Locate every white blood cell.
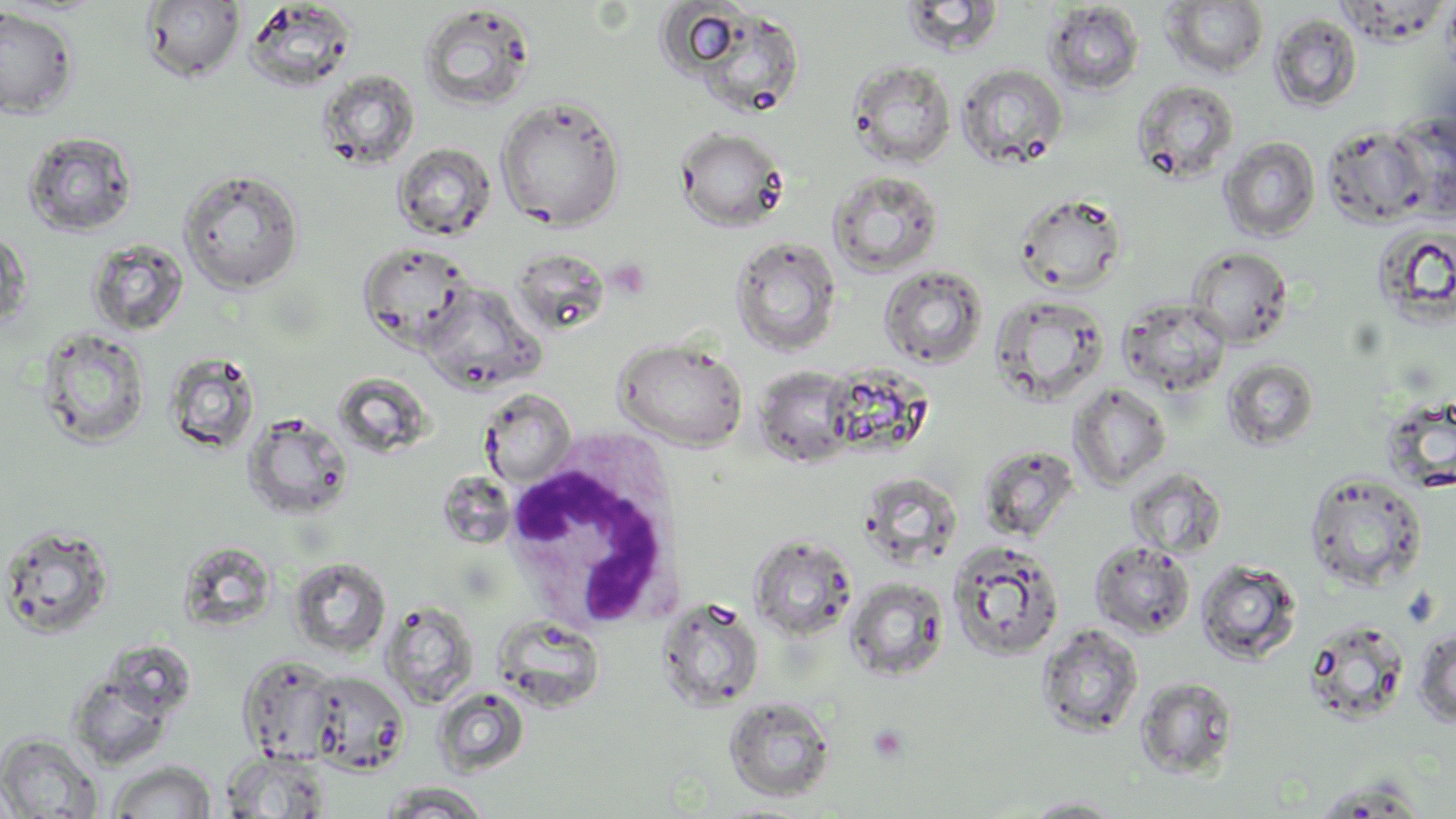
Approximate bounding boxes as (x1,y1)-(x2,y2) corner pairs in pixels.
White blood cells: (503,429)-(687,633).

slide-level diagnosis = no evidence of blood parasites
magnification = 1000x
stain = May-Grünwald-Giemsa
preparation = thin blood film
image size = 1456×819 pixels
field of view = one of a larger specimen
uninfected red blood cell locations = approximate bounding boxes as (x1,y1)-(x2,y2) corner pairs in pixels: (141,1)-(246,84), (244,1)-(358,94), (899,1)-(1007,57), (1161,1)-(1269,79), (1043,2)-(1145,95), (654,3)-(752,80), (417,4)-(537,112), (0,6)-(79,119), (683,7)-(807,119), (1269,13)-(1363,112), (847,59)-(956,169), (956,63)-(1068,170), (316,69)-(420,170), (1131,79)-(1240,184), (495,96)-(626,230), (1388,111)-(1456,220), (1321,125)-(1428,227), (673,126)-(789,231), (22,130)-(138,238), (1219,137)-(1320,241), (393,143)-(496,241), (178,168)-(305,294), (827,170)-(944,278), (1014,191)-(1128,295), (1372,224)-(1456,328), (0,226)-(33,333), (729,236)-(842,357), (86,238)-(189,337), (357,241)-(475,351), (1187,246)-(1294,349), (508,247)-(609,335), (878,265)-(989,370), (420,281)-(544,394), (989,292)-(1110,405), (1118,297)-(1231,396), (37,327)-(151,449), (613,337)-(749,451), (163,351)-(262,456), (1221,357)-(1320,451), (753,366)-(858,467), (1068,383)-(1172,491), (478,388)-(577,487), (1381,396)-(1456,493), (243,413)-(355,521), (977,444)-(1080,541), (1124,466)-(1227,560), (1303,471)-(1428,592), (859,473)-(963,568), (0,522)-(117,641), (747,533)-(858,642), (947,539)-(1065,659), (1089,540)-(1196,639), (289,557)-(391,658), (1196,559)-(1302,665), (844,577)-(949,682), (656,597)-(765,713), (382,602)-(479,708), (492,614)-(606,712), (1302,619)-(1412,726), (1037,624)-(1144,738), (1412,628)-(1456,727), (239,655)-(343,764), (68,669)-(177,771), (304,670)-(410,774), (1135,676)-(1239,778), (432,686)-(530,777), (723,696)-(837,803), (0,732)-(103,817), (221,750)-(332,818), (107,760)-(218,818), (1310,777)-(1430,817), (379,782)-(494,817), (1022,796)-(1128,817)
modality = optical microscopy
platelet locations = approximate bounding boxes as (x1,y1)-(x2,y2) corner pairs in pixels: (607,256)-(653,298), (1401,586)-(1440,628), (868,724)-(909,766)